Give the extent of all Plasmodium vivax-infected red blood cells.
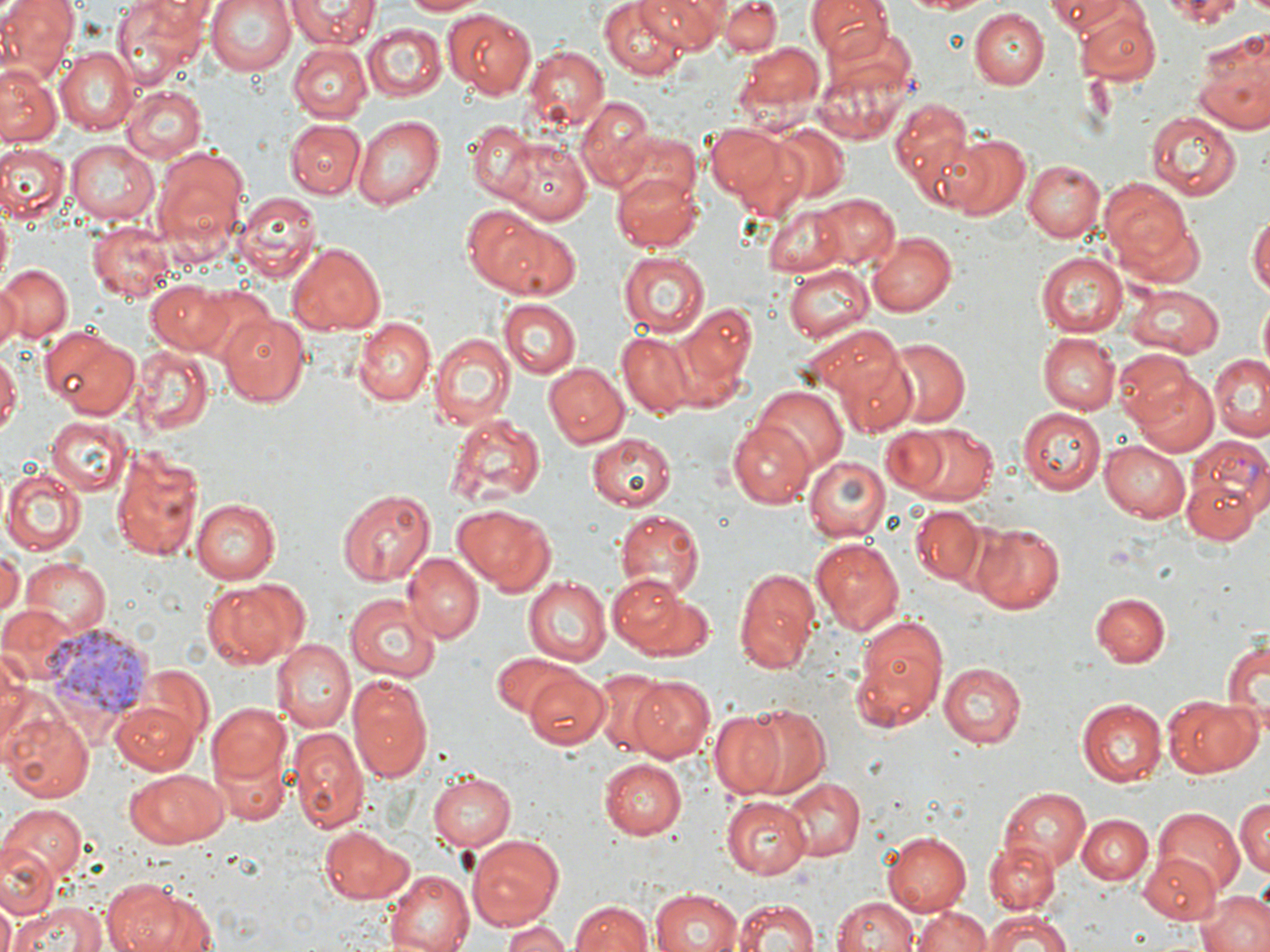

Approximate bounding boxes as [x1, y1, x2, y2] in pixels.
Plasmodium vivax-infected red blood cells: [1183, 436, 1270, 531], [41, 625, 157, 717].

slide_level_diagnosis: Plasmodium vivax
uninfected_red_blood_cell_locations: 'approximate bounding boxes as [x1, y1, x2, y2] in pixels: [0, 0, 77, 82], [114, 0, 211, 82], [203, 0, 299, 77], [288, 0, 377, 48], [397, 0, 484, 16], [600, 0, 690, 79], [634, 0, 724, 51], [721, 0, 782, 56], [807, 0, 890, 56], [892, 0, 996, 15], [1047, 0, 1134, 35], [1149, 0, 1256, 24], [445, 8, 539, 97], [969, 9, 1049, 88], [1074, 9, 1160, 86], [362, 23, 446, 101], [1193, 28, 1270, 134], [739, 40, 826, 121], [288, 43, 372, 122], [57, 46, 138, 134], [520, 46, 608, 133], [812, 53, 917, 148], [1170, 64, 1265, 195], [0, 67, 58, 147], [121, 86, 206, 162], [576, 95, 655, 187], [888, 96, 979, 204], [1147, 110, 1242, 199], [353, 114, 446, 210], [284, 119, 364, 198], [467, 120, 534, 205], [707, 124, 794, 206], [773, 125, 850, 203], [944, 134, 1030, 220], [67, 139, 157, 226], [501, 140, 592, 224], [0, 144, 68, 221], [153, 151, 247, 245], [1024, 159, 1105, 241], [1018, 167, 1178, 249], [613, 168, 705, 251], [1100, 180, 1197, 276], [235, 191, 321, 281], [812, 194, 901, 271], [463, 204, 562, 294], [762, 204, 852, 277], [1248, 208, 1270, 302], [1119, 212, 1208, 291], [90, 222, 173, 299], [493, 225, 581, 300], [868, 231, 957, 317], [288, 242, 386, 333], [618, 250, 710, 337], [1036, 251, 1127, 338], [785, 264, 874, 343], [0, 265, 73, 345], [0, 280, 23, 350], [147, 280, 231, 355], [1125, 286, 1222, 359], [500, 298, 582, 378], [670, 301, 758, 404], [216, 311, 310, 407], [353, 316, 434, 405], [38, 326, 139, 419], [427, 330, 514, 431], [1040, 332, 1120, 414], [617, 333, 699, 417], [884, 338, 971, 426], [838, 344, 920, 437], [135, 347, 213, 436], [1113, 350, 1203, 431], [0, 351, 21, 438], [1208, 355, 1270, 443], [542, 361, 628, 449], [1132, 373, 1219, 456], [751, 383, 849, 477], [1018, 406, 1105, 495], [447, 411, 546, 507], [46, 416, 133, 496], [727, 421, 815, 507], [897, 421, 1001, 506], [585, 433, 675, 512], [1099, 440, 1190, 523], [108, 444, 206, 562], [806, 456, 888, 542], [2, 468, 86, 555], [1184, 477, 1257, 543], [335, 488, 436, 585], [190, 496, 282, 583], [453, 504, 556, 593], [911, 506, 989, 588], [614, 509, 705, 597], [971, 523, 1066, 613], [811, 538, 906, 635], [0, 547, 21, 620], [403, 553, 484, 642], [19, 559, 110, 638], [733, 564, 821, 674], [608, 572, 692, 655], [523, 576, 611, 666], [200, 578, 302, 669], [1092, 592, 1170, 667], [344, 593, 440, 683], [849, 616, 948, 733], [1224, 634, 1269, 729], [271, 638, 353, 732], [489, 650, 585, 720], [936, 660, 1025, 749], [141, 664, 211, 743], [523, 669, 610, 749], [586, 672, 668, 752], [347, 674, 434, 783], [626, 676, 716, 763], [1166, 697, 1262, 776], [1076, 698, 1165, 787], [109, 699, 200, 773], [206, 702, 291, 788], [737, 703, 833, 802], [2, 707, 92, 804], [709, 709, 795, 801], [289, 725, 367, 833], [598, 758, 687, 839], [124, 768, 228, 848], [429, 772, 516, 851], [780, 776, 865, 862], [997, 786, 1090, 876], [1233, 794, 1269, 880], [721, 796, 814, 878], [1, 805, 85, 889], [1152, 809, 1245, 899], [1080, 814, 1152, 885], [320, 824, 416, 905], [882, 830, 971, 916], [468, 834, 562, 931], [986, 843, 1059, 913], [0, 845, 56, 921], [1139, 852, 1223, 926], [387, 869, 475, 952], [103, 879, 190, 952], [649, 888, 745, 952], [1195, 888, 1270, 952], [832, 895, 920, 952], [567, 898, 656, 951], [733, 898, 819, 952], [11, 900, 102, 952], [914, 906, 988, 952], [977, 912, 1078, 951], [501, 918, 572, 952]'
image_size: 1270×952 pixels
field_of_view: single
magnification: 1000x
preparation: thin blood smear
stain: May-Grünwald-Giemsa
modality: optical microscopy